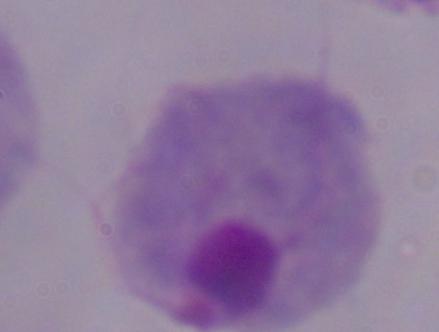
1000x magnification. Micrograph. A trichomonad is seen.